Report the malaria status.
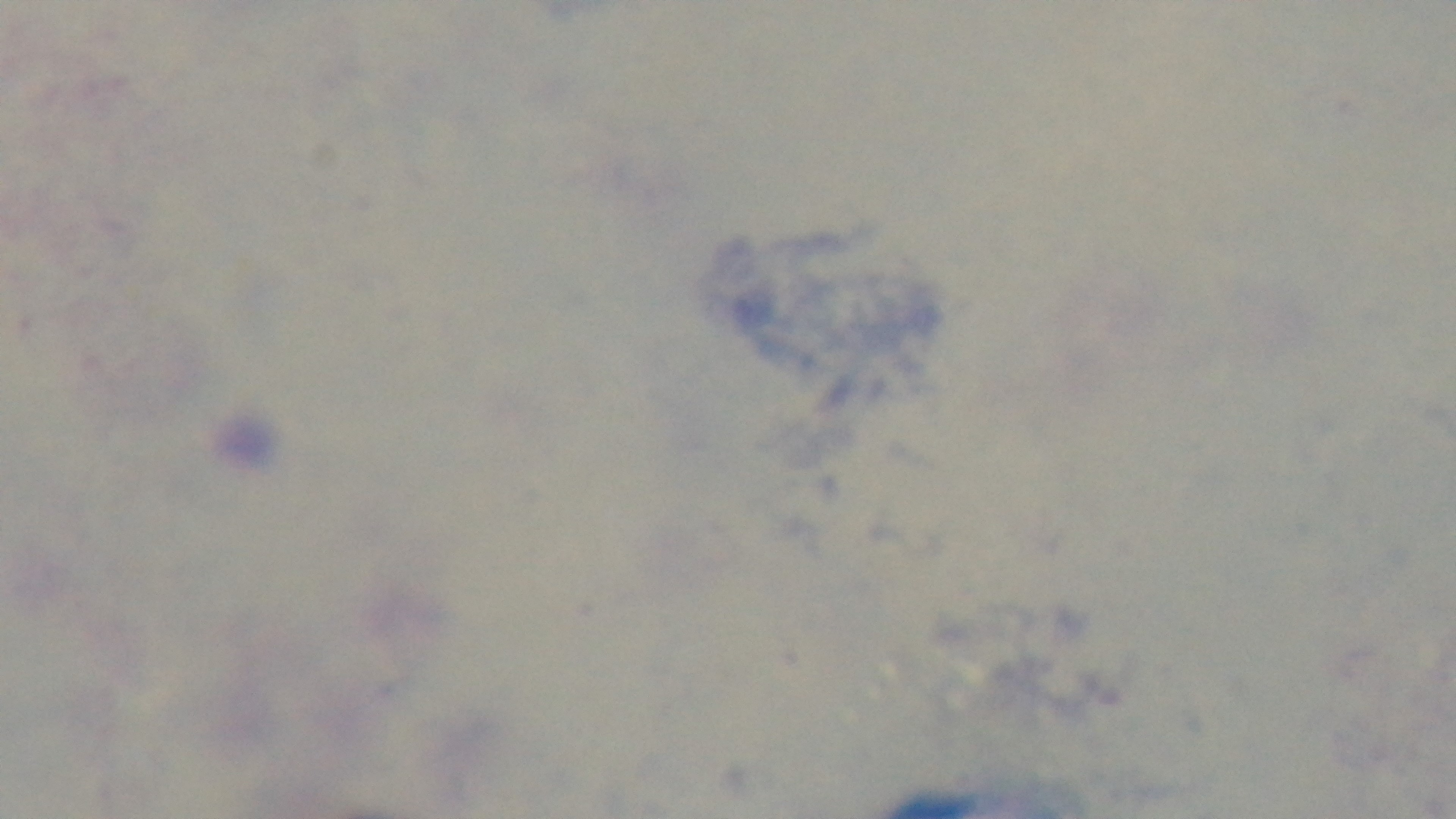
Uninfected.

Summary:
  - Field of view: one from the slide
  - Objective: 100x oil immersion
  - Preparation: thick
  - Modality: light microscopy
  - Capture: mounted 4K digital camera
  - Stain: Giemsa